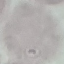
{
  "malaria_status": "uninfected",
  "stain": "Giemsa",
  "capture": "smartphone through the microscope eyepiece",
  "preparation": "thin blood film",
  "image_type": "cell patch, automatically extracted from a larger field of view and resized to 64 × 64 pixels"
}